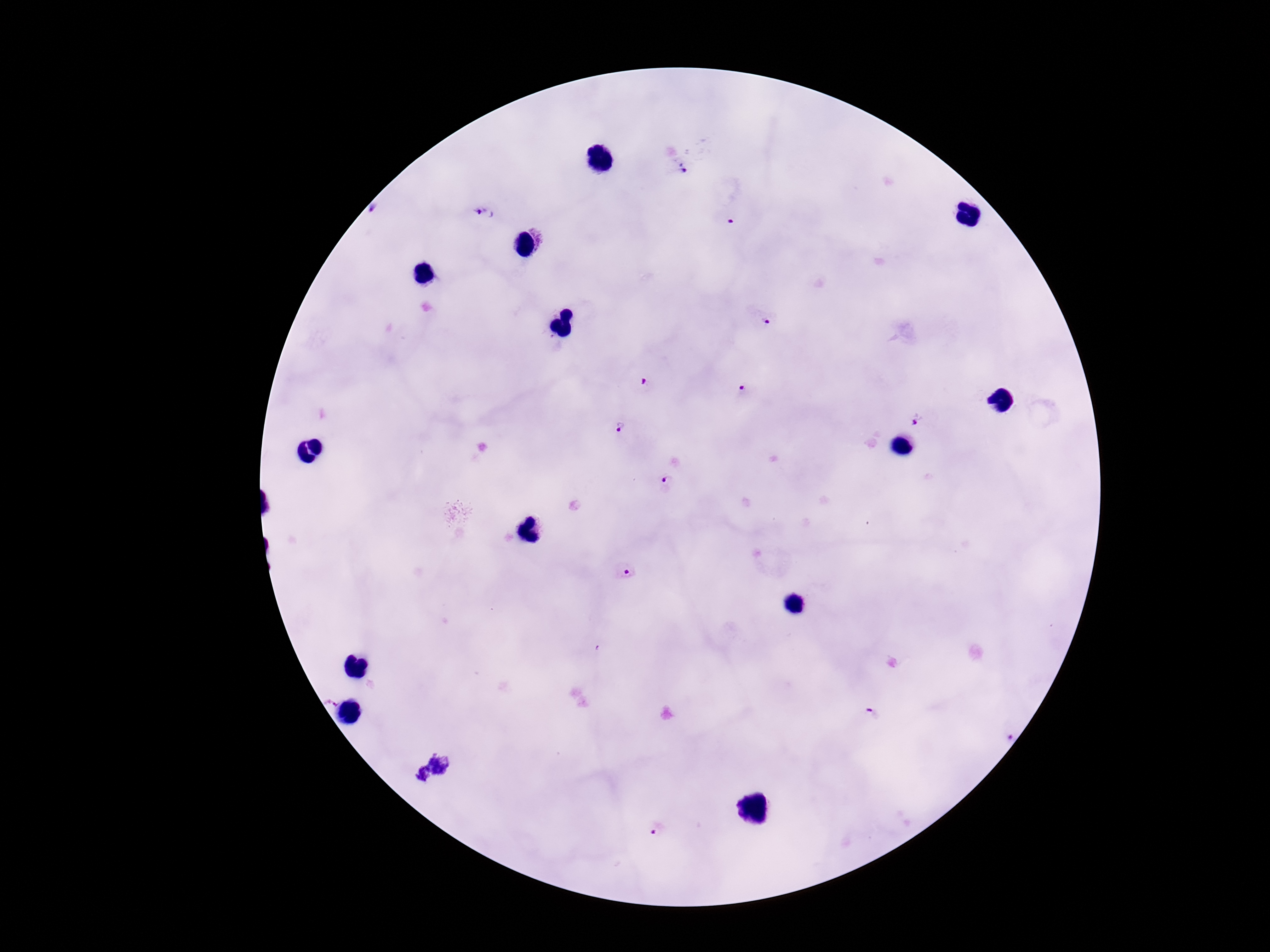

Approximate centers as {x, y} in pixels.
Summary:
  - Plasmodium parasite locations: {679, 164}, {484, 213}, {730, 221}, {765, 321}, {646, 384}, {742, 388}, {917, 420}, {620, 428}, {665, 480}, {628, 571}, {867, 716}, {1005, 735}, {656, 827}
  - Patient malaria status: positive
  - Magnification: 100x
  - Preparation: thick blood film
  - Stain: Giemsa
  - Image size: 1270×952 pixels
  - Field of view: single
  - Capture: smartphone camera through the microscope eyepiece